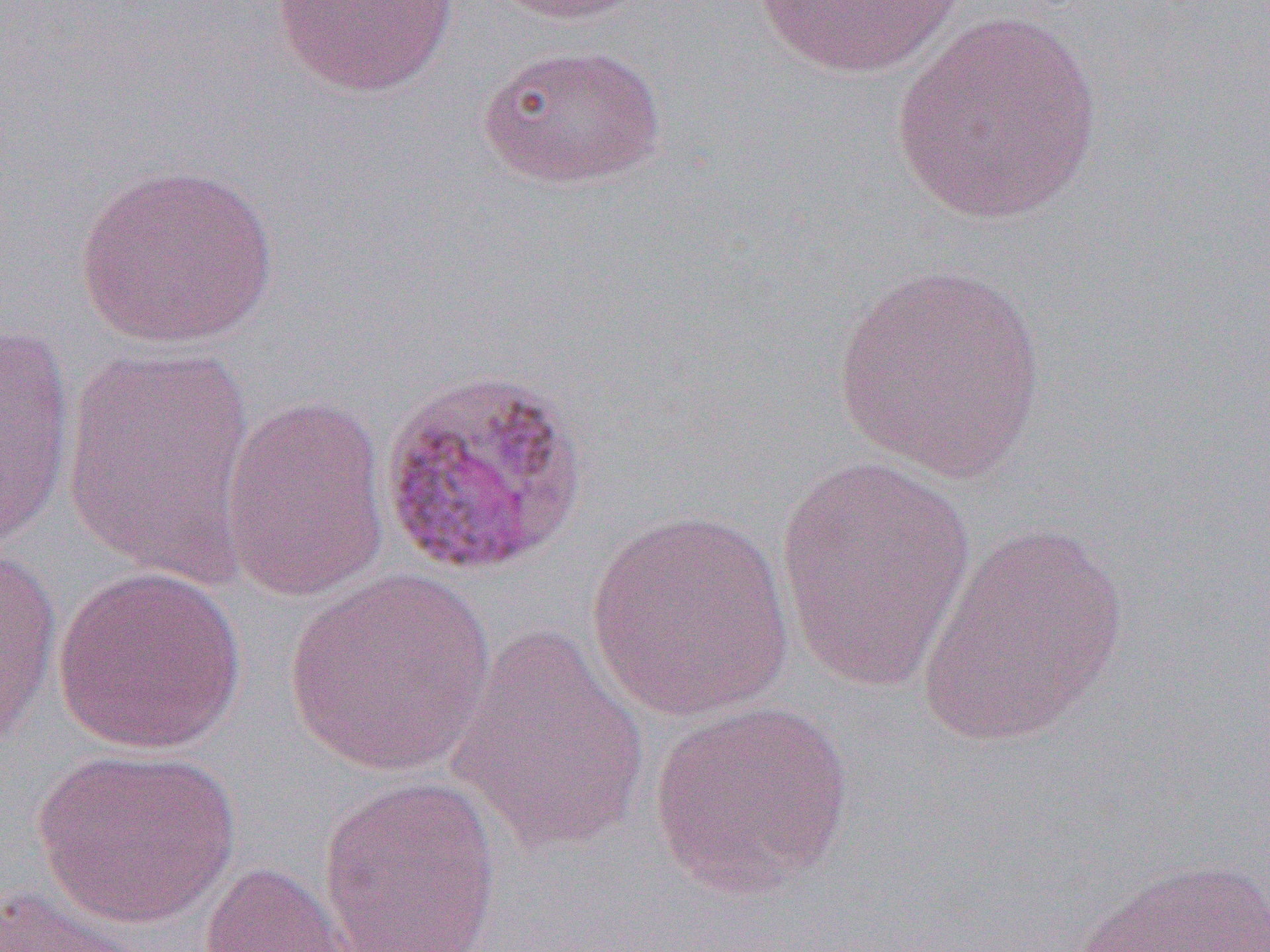

{
  "slide_level_diagnosis": "Plasmodium malariae",
  "modality": "optical microscopy",
  "magnification": "1000x",
  "field_of_view": "single",
  "preparation": "thin blood film",
  "uninfected_red_blood_cell_locations": "approximate bounding boxes as [x1, y1, x2, y2] in pixels: [272, 0, 460, 98], [488, 0, 658, 26], [752, 0, 966, 80], [889, 13, 1103, 226], [475, 43, 667, 190], [76, 163, 279, 350], [830, 263, 1049, 483], [0, 322, 76, 552], [60, 340, 258, 585], [221, 396, 391, 603], [773, 454, 975, 694], [583, 510, 797, 722], [914, 522, 1132, 748], [0, 545, 63, 750], [51, 565, 247, 754], [281, 569, 498, 778], [446, 624, 652, 852], [647, 700, 856, 899], [30, 747, 242, 929], [317, 775, 502, 952], [1067, 856, 1270, 952], [198, 860, 361, 952], [0, 884, 150, 952]",
  "image_size": "1270×952 pixels"
}